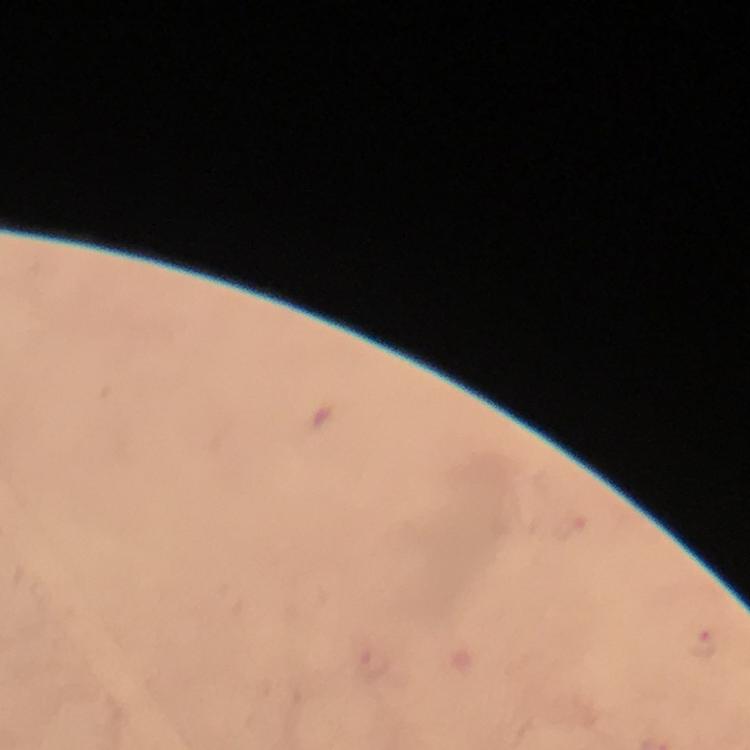

Approximate object centers, in pixels from the top-left corner. Plasmodium parasite locations: (x=706, y=644). Cropped region of a single field of view. From a malaria diagnostic workup. At 100x magnification. Photographed with a smartphone mounted on the microscope. Thick smear. Image is 750×750 pixels. Giemsa stain. Immersion oil was used.